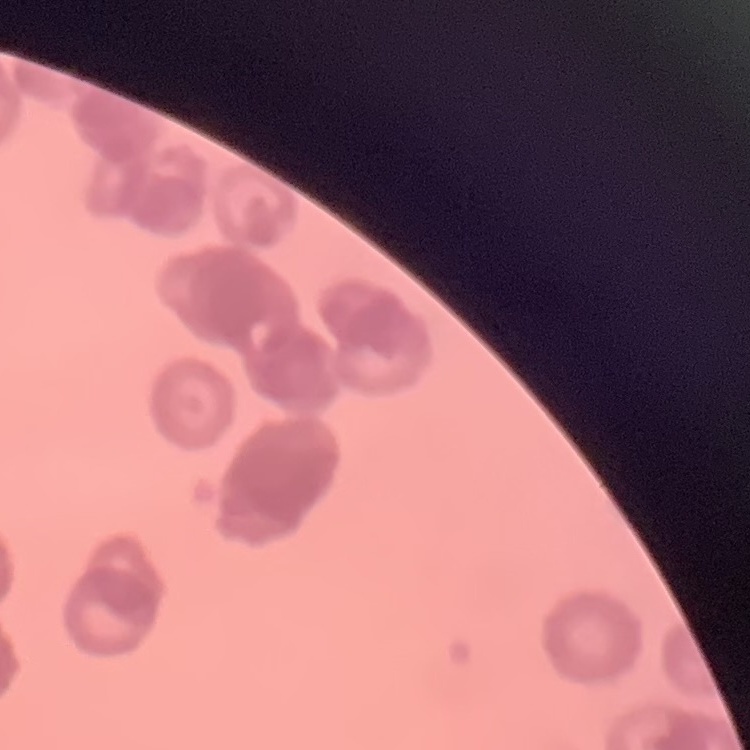

erythrocyte morphology = rouleaux formation
image type = one tile cut from a larger photomicrograph
preparation = thin blood smear
stain = Field's or Giemsa